Assess the morphology of the erythrocytes.
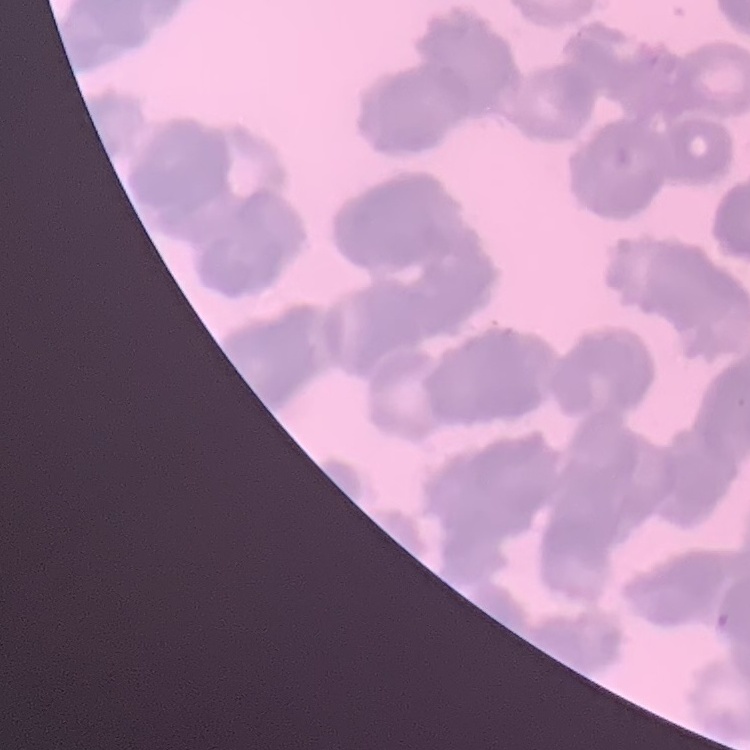
Rouleaux formation.

preparation = thin blood film
stain = Field's or Giemsa
image type = one tile cut from a larger photomicrograph